Classify this cell by malaria status.
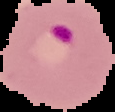

It is parasitized.

{
  "preparation": "thin blood smear",
  "image_size": "115×112 pixels",
  "image_type": "cell region segmented out of the field of view; surrounding area masked to black"
}